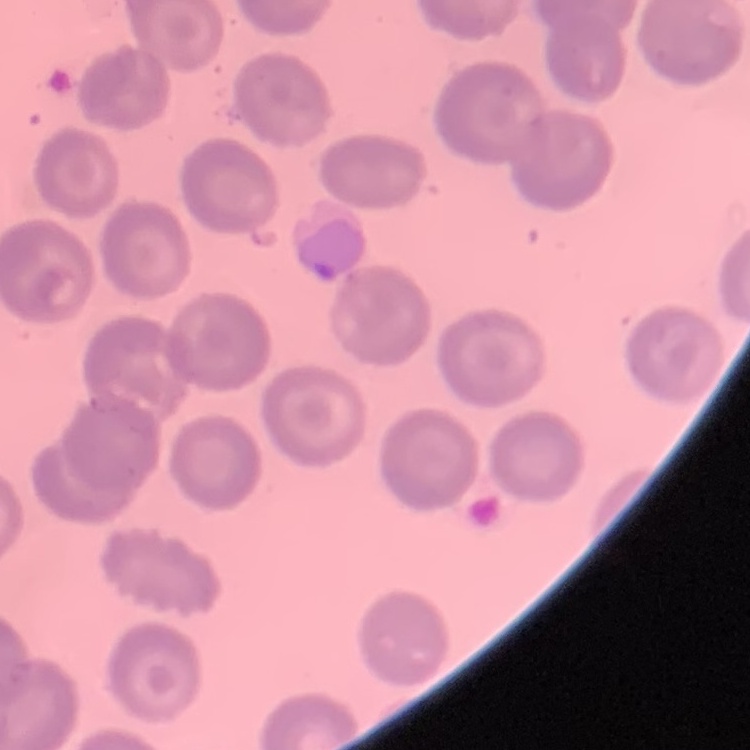

{
  "red_blood_cell_morphology": "no rouleaux formation",
  "preparation": "thin blood film",
  "image_type": "square crop of a larger photomicrograph",
  "stain": "Field's or Giemsa"
}